Assess the morphology of the erythrocytes.
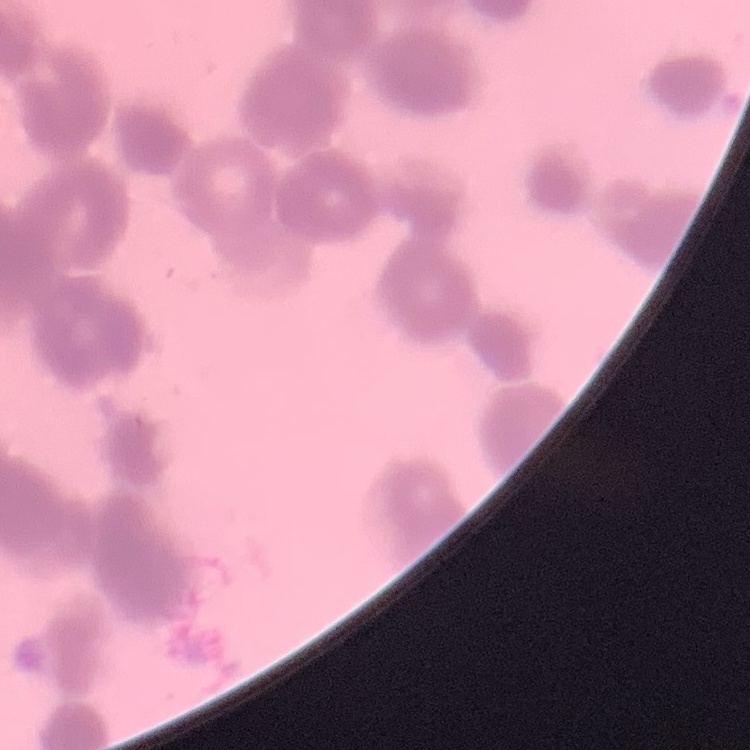
They show rouleaux formation.

stain = Field's or Giemsa
image type = square crop of a larger photomicrograph
preparation = thin peripheral smear